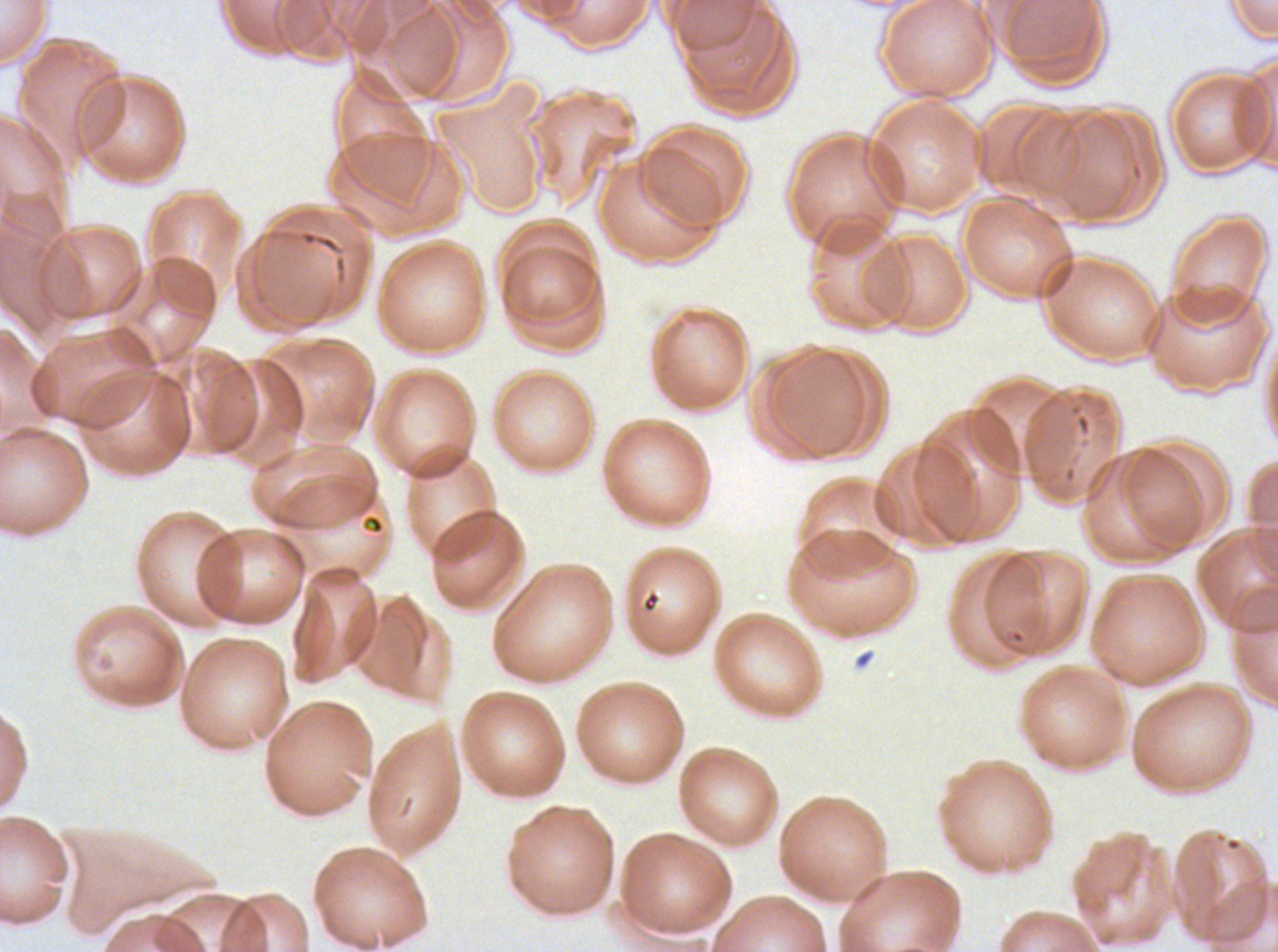 Approximate bounding boxes as {x1, y1, x2, y2} in pixels. Debris locations: {297, 228, 343, 255}. Thin blood film. One sub-image of a larger composite. Image is 1278×952 pixels. P. falciparum cultured ex vivo for 24 to 48 hours, from a patient in The Gambia. Giemsa-stained preparation.